Locate every blood parasite and identify its species.
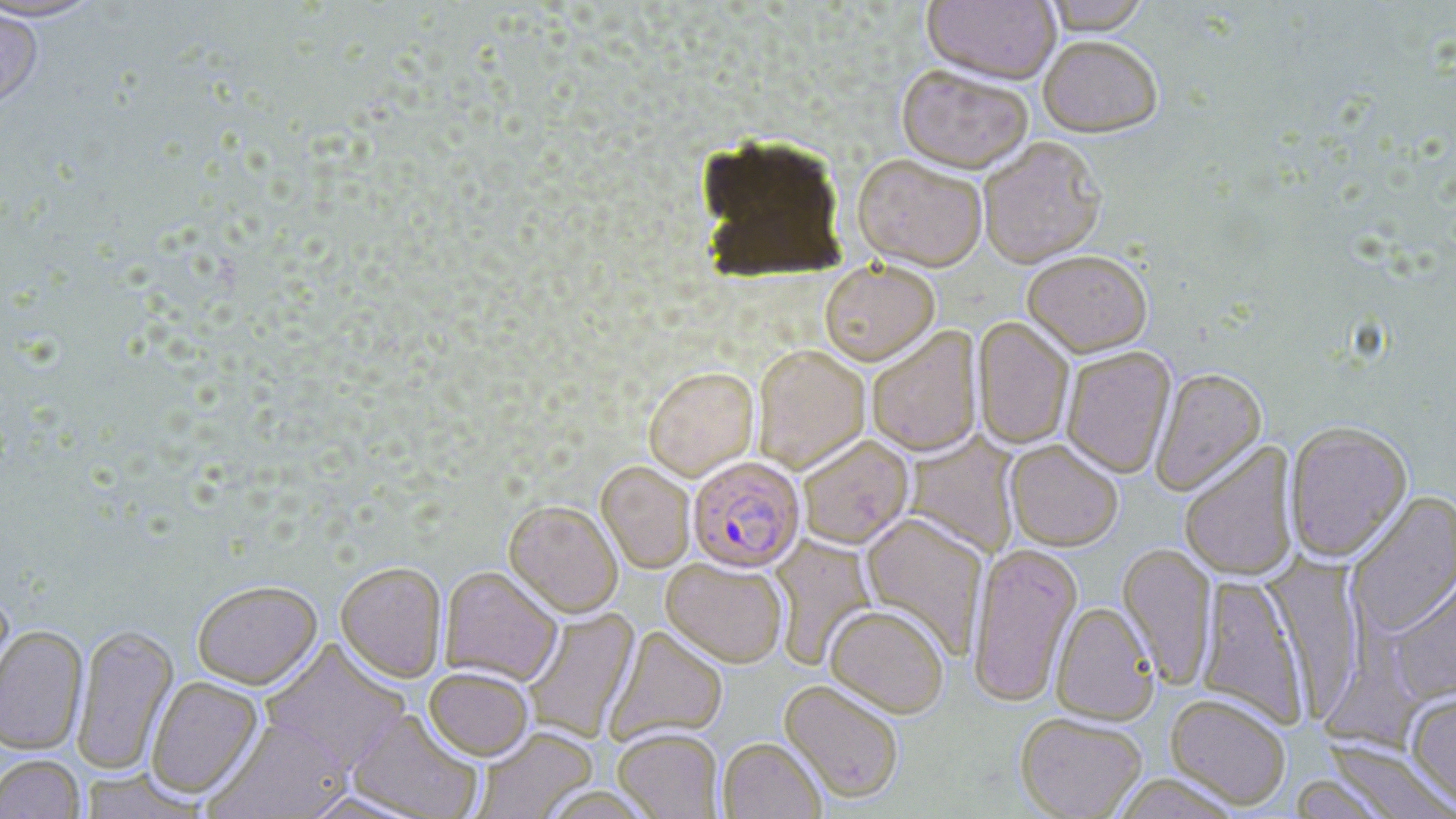
Approximate bounding boxes as [x1, y1, x2, y2] in pixels.
Plasmodium falciparum-infected red blood cells: [691, 455, 809, 572].
No Plasmodium ovale, Plasmodium malariae, Plasmodium vivax, Babesia divergens, or Trypanosoma brucei observed.

slide_level_diagnosis: Plasmodium falciparum
field_of_view: single
stain: May-Grünwald-Giemsa
image_size: 1456×819 pixels
magnification: 1000x
uninfected_red_blood_cell_locations: 'approximate bounding boxes as [x1, y1, x2, y2] in pixels: [0, 0, 105, 24], [921, 0, 1060, 88], [1041, 0, 1152, 39], [0, 6, 45, 113], [1038, 39, 1162, 141], [895, 69, 1033, 178], [978, 138, 1107, 272], [851, 157, 987, 275], [1023, 253, 1153, 360], [819, 262, 940, 369], [972, 318, 1074, 450], [867, 328, 983, 458], [753, 346, 870, 473], [1061, 348, 1177, 480], [643, 367, 759, 482], [1149, 368, 1267, 498], [1284, 423, 1412, 564], [905, 432, 1021, 559], [798, 436, 914, 551], [1005, 441, 1123, 553], [1180, 443, 1301, 583], [596, 462, 695, 575], [1345, 491, 1456, 638], [503, 502, 623, 619], [860, 514, 989, 660], [768, 534, 878, 670], [1117, 543, 1218, 690], [967, 545, 1083, 710], [1261, 552, 1368, 722], [660, 558, 788, 670], [335, 563, 447, 684], [439, 567, 563, 687], [1387, 574, 1456, 705], [1196, 575, 1309, 730], [192, 581, 322, 691], [0, 591, 15, 707], [1050, 604, 1159, 726], [824, 607, 950, 721], [522, 608, 641, 743], [71, 624, 179, 775], [0, 625, 89, 756], [605, 627, 728, 746], [259, 640, 411, 775], [423, 669, 533, 762], [146, 677, 264, 800], [778, 681, 903, 805], [1405, 692, 1456, 810], [1165, 695, 1290, 811], [346, 709, 484, 819], [1015, 715, 1148, 819], [204, 718, 355, 819], [474, 727, 598, 819], [613, 730, 724, 819], [718, 739, 825, 819], [1323, 741, 1454, 818], [0, 755, 85, 819], [78, 770, 206, 818], [1112, 774, 1241, 818], [1287, 774, 1395, 819]'
preparation: thin blood film
modality: light microscopy